Report the malaria status of this cell.
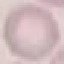

It is uninfected.

{
  "capture": "smartphone camera at the microscope eyepiece",
  "image_type": "cell patch, automatically extracted from a larger field of view and resized to 64 × 64 pixels",
  "preparation": "thin blood smear",
  "stain": "Giemsa"
}